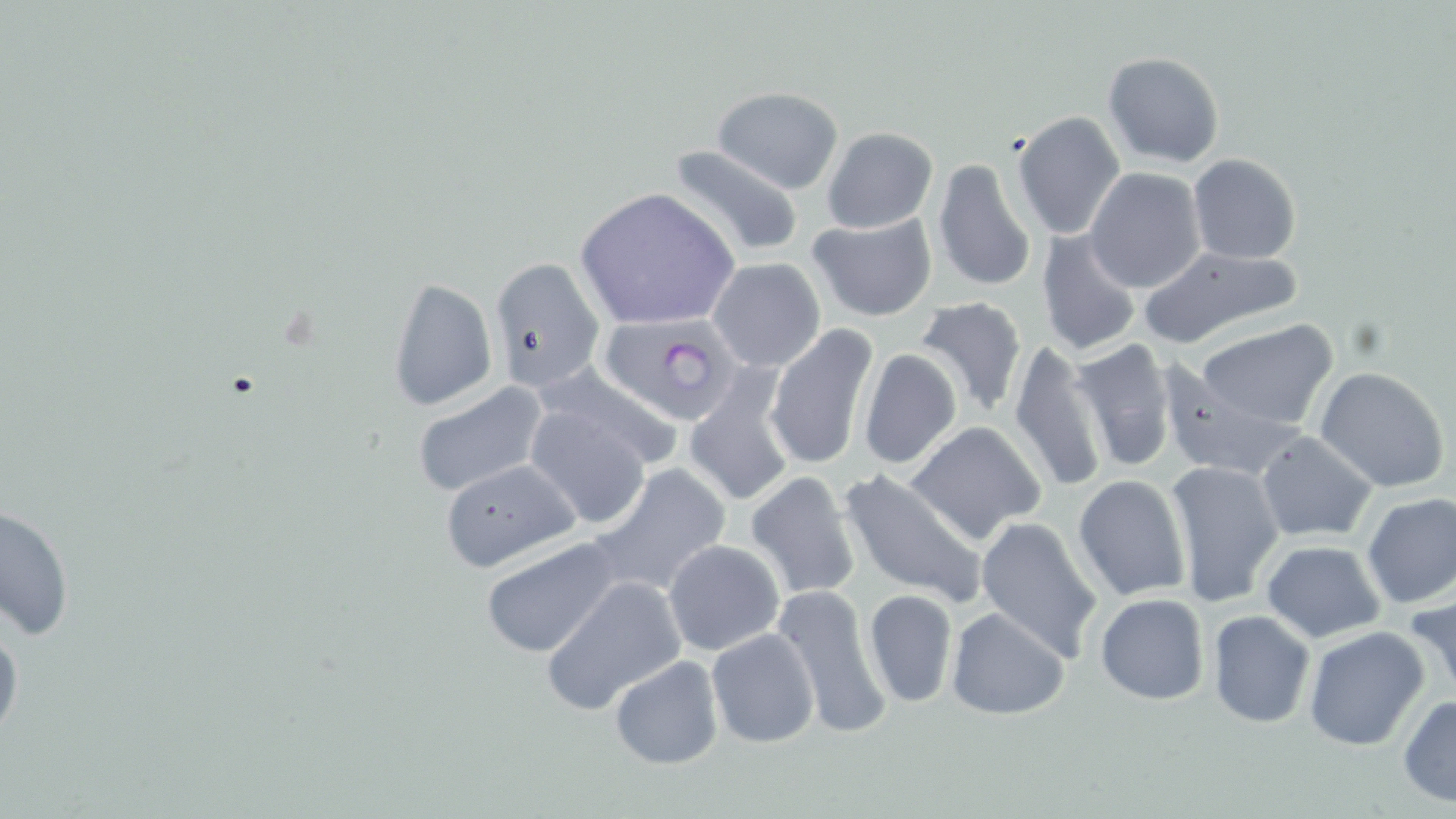 Approximate bounding boxes as (x1, y1, x2, y2) in pixels. Uninfected red blood cell locations: (1101, 52, 1226, 169), (713, 87, 842, 193), (1011, 110, 1126, 240), (822, 126, 938, 233), (666, 143, 805, 263), (1188, 154, 1301, 264), (931, 157, 1038, 294), (1086, 167, 1206, 293), (573, 187, 740, 330), (805, 213, 939, 322), (1034, 227, 1143, 358), (1135, 244, 1306, 349), (488, 256, 605, 395), (708, 257, 826, 372), (386, 277, 497, 412), (912, 296, 1029, 421), (1195, 320, 1338, 432), (768, 324, 880, 476), (1068, 338, 1180, 475), (1006, 340, 1108, 493), (857, 347, 964, 475), (534, 363, 685, 473), (1160, 365, 1310, 481), (1315, 367, 1450, 493), (681, 371, 799, 510), (410, 380, 548, 499), (524, 403, 652, 529), (902, 419, 1049, 546), (1255, 430, 1379, 543), (438, 457, 581, 573), (1165, 460, 1284, 608), (588, 463, 732, 599), (837, 465, 989, 610), (744, 470, 862, 602), (1071, 474, 1193, 603), (1360, 493, 1456, 610), (2, 499, 74, 644), (975, 516, 1104, 663), (477, 536, 629, 660), (662, 538, 787, 657), (1259, 539, 1388, 643), (540, 575, 686, 716), (770, 582, 892, 741), (863, 588, 958, 709), (1407, 590, 1456, 703), (1095, 593, 1210, 706), (947, 606, 1071, 721), (1207, 610, 1315, 728), (0, 611, 23, 750), (1304, 626, 1431, 750), (705, 627, 820, 749), (609, 656, 723, 770), (1398, 693, 1456, 806). Plasmodium falciparum-infected red blood cell locations: (598, 313, 746, 427). Slide-level diagnosis: Plasmodium falciparum. Captured at 1000x magnification. Light microscopy. Image is 1456×819 pixels. May-Grünwald-Giemsa stain. Thin blood film. One field of a larger specimen.